Classify this cell by malaria status.
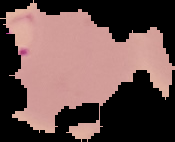

Parasitized.

Summary:
  - Image size: 175×142 pixels
  - Preparation: thin blood smear
  - Image type: segmented cell region on a black background